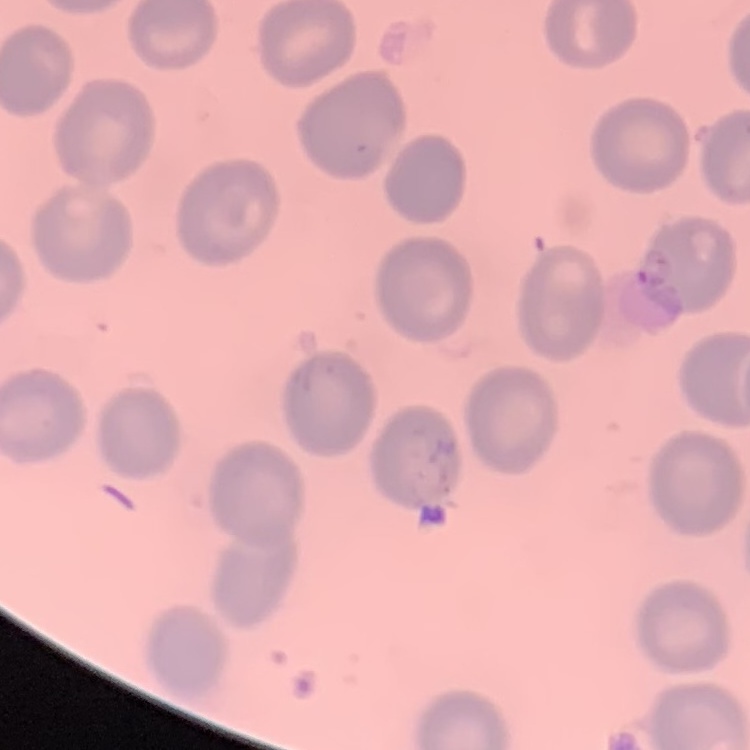
Summary:
  - Erythrocyte morphology: no rouleaux formation
  - Stain: Field's or Giemsa
  - Image type: square crop of a larger photomicrograph
  - Preparation: thin blood film